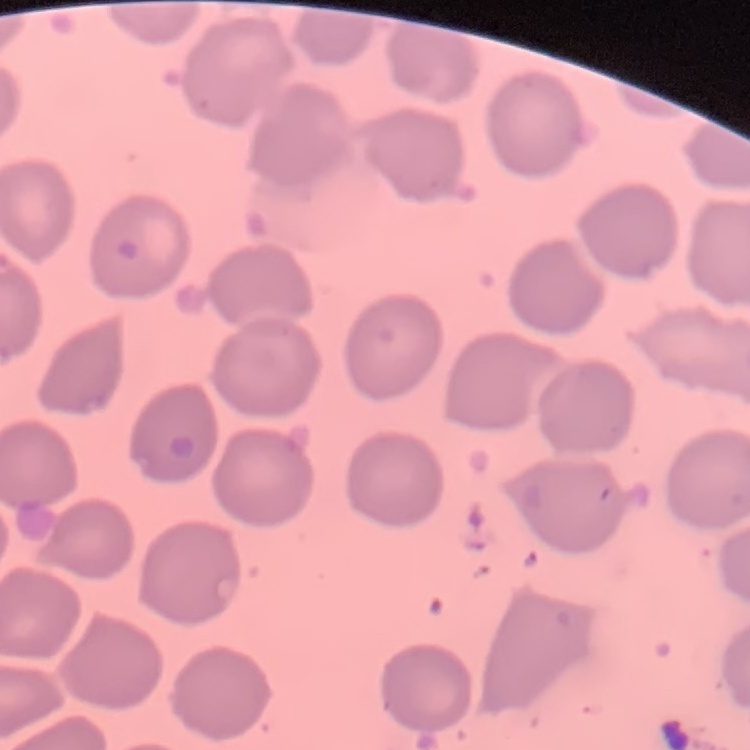
Summary:
  - Erythrocyte morphology: no rouleaux formation
  - Stain: Field's or Giemsa
  - Image type: square crop of a larger photomicrograph
  - Preparation: thin blood smear